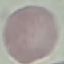

malaria status = uninfected
preparation = thin smear
capture = smartphone through the microscope eyepiece
stain = Giemsa
image type = cell patch, automatically extracted from a larger field of view and resized to 64 × 64 pixels